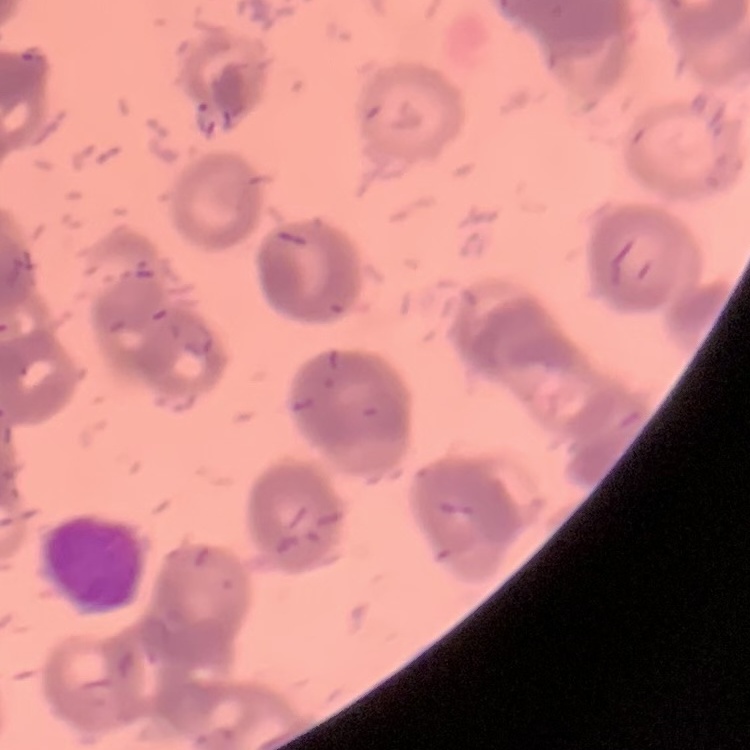

Summary:
  - Red blood cell morphology: rouleaux formation
  - Image type: square crop of a larger photomicrograph
  - Preparation: thin blood smear
  - Stain: Field's or Giemsa